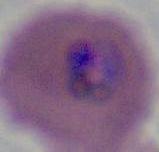

modality = micrograph
magnification = 400x or 1000x
identification = Plasmodium